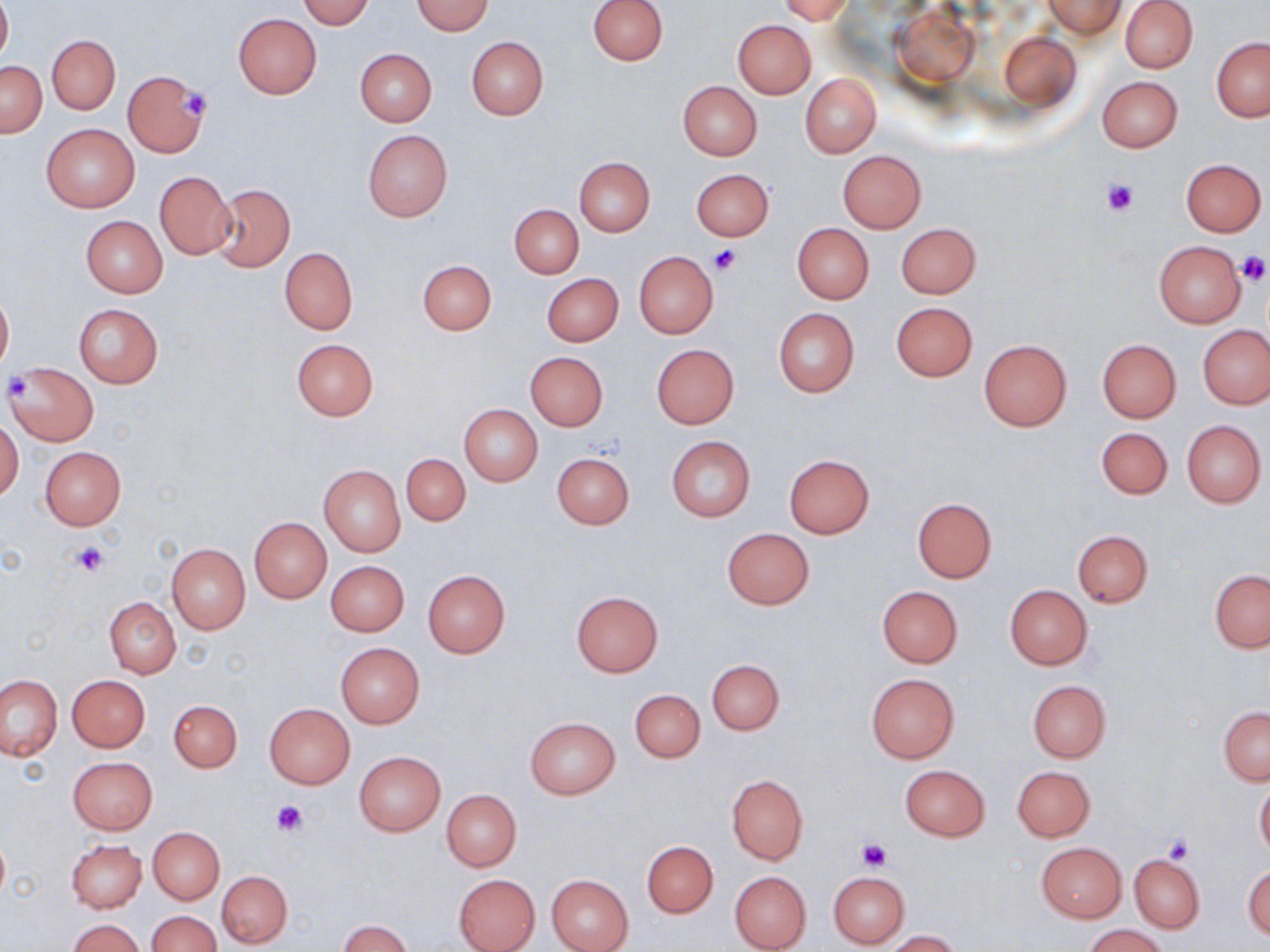

Approximate bounding boxes as (x1, y1, x2, y2) in pixels. Uninfected red blood cell locations: (299, 0, 374, 29), (589, 0, 667, 65), (778, 0, 856, 24), (1043, 0, 1126, 39), (1120, 0, 1198, 73), (0, 1, 11, 65), (412, 1, 494, 35), (233, 13, 322, 99), (733, 20, 815, 98), (998, 31, 1080, 111), (46, 35, 120, 114), (466, 37, 549, 119), (1211, 38, 1270, 122), (354, 49, 436, 126), (0, 60, 46, 137), (123, 71, 208, 157), (800, 73, 881, 158), (1098, 76, 1183, 152), (677, 81, 762, 161), (41, 122, 140, 213), (363, 130, 452, 221), (837, 150, 926, 234), (574, 156, 655, 235), (1180, 158, 1266, 236), (691, 169, 773, 241), (154, 172, 236, 259), (209, 184, 296, 272), (510, 205, 582, 278), (81, 216, 167, 298), (895, 222, 981, 298), (792, 223, 874, 304), (1154, 240, 1247, 328), (280, 247, 358, 335), (633, 251, 719, 338), (418, 259, 497, 334), (542, 273, 623, 346), (0, 287, 13, 376), (891, 302, 977, 382), (73, 303, 164, 388), (773, 309, 859, 396), (1199, 327, 1269, 409), (1097, 338, 1181, 424), (292, 339, 379, 420), (979, 339, 1072, 431), (652, 345, 739, 428), (525, 352, 609, 430), (6, 363, 99, 445), (459, 404, 543, 487), (1182, 419, 1266, 507), (0, 420, 25, 501), (1096, 427, 1172, 500), (667, 436, 756, 520), (40, 447, 126, 529), (552, 452, 635, 529), (401, 454, 470, 525), (784, 455, 874, 538), (319, 465, 405, 556), (912, 499, 997, 581), (250, 518, 331, 602), (722, 528, 814, 610), (1073, 530, 1153, 607), (167, 543, 250, 634), (327, 561, 409, 636), (422, 569, 510, 659), (1210, 569, 1270, 652), (1004, 585, 1093, 670), (876, 586, 963, 668), (572, 591, 663, 676), (105, 597, 180, 678), (335, 643, 425, 729), (707, 659, 784, 734), (866, 673, 958, 763), (67, 674, 150, 752), (0, 675, 63, 761), (1026, 679, 1111, 763), (629, 688, 706, 764), (169, 699, 242, 771), (264, 703, 356, 790), (1219, 707, 1269, 785), (526, 717, 620, 800), (354, 751, 445, 834), (67, 756, 157, 833), (899, 764, 990, 841), (1012, 766, 1094, 842), (727, 776, 808, 864), (1255, 780, 1270, 860), (442, 789, 521, 871), (149, 827, 224, 904), (0, 831, 9, 905), (67, 838, 147, 913), (642, 841, 718, 918), (1036, 842, 1126, 923), (1130, 852, 1205, 933), (1243, 862, 1270, 941), (729, 870, 811, 951), (218, 871, 291, 947), (828, 871, 909, 949), (452, 873, 540, 952), (546, 874, 634, 952), (149, 911, 221, 952), (68, 919, 145, 951), (338, 920, 412, 952), (1084, 924, 1167, 952), (885, 931, 962, 951). Platelet locations: (180, 90, 213, 121), (1099, 177, 1141, 218), (710, 244, 742, 275), (1235, 251, 1269, 286), (6, 372, 34, 400), (72, 541, 111, 575), (272, 801, 306, 837), (1163, 836, 1193, 862), (856, 837, 892, 871). Slide-level diagnosis: negative for blood parasites. Captured at 1000x magnification. Single field of view. Thin blood smear. May-Grünwald-Giemsa stain. Image is 1270×952 pixels. Light microscopy.